Report the malaria status of this cell.
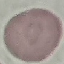

Uninfected.

Cell patch, automatically extracted from a larger field of view and resized to 64 × 64 pixels. Photographed with a smartphone camera at the microscope eyepiece. Giemsa-stained preparation. Thin blood film.